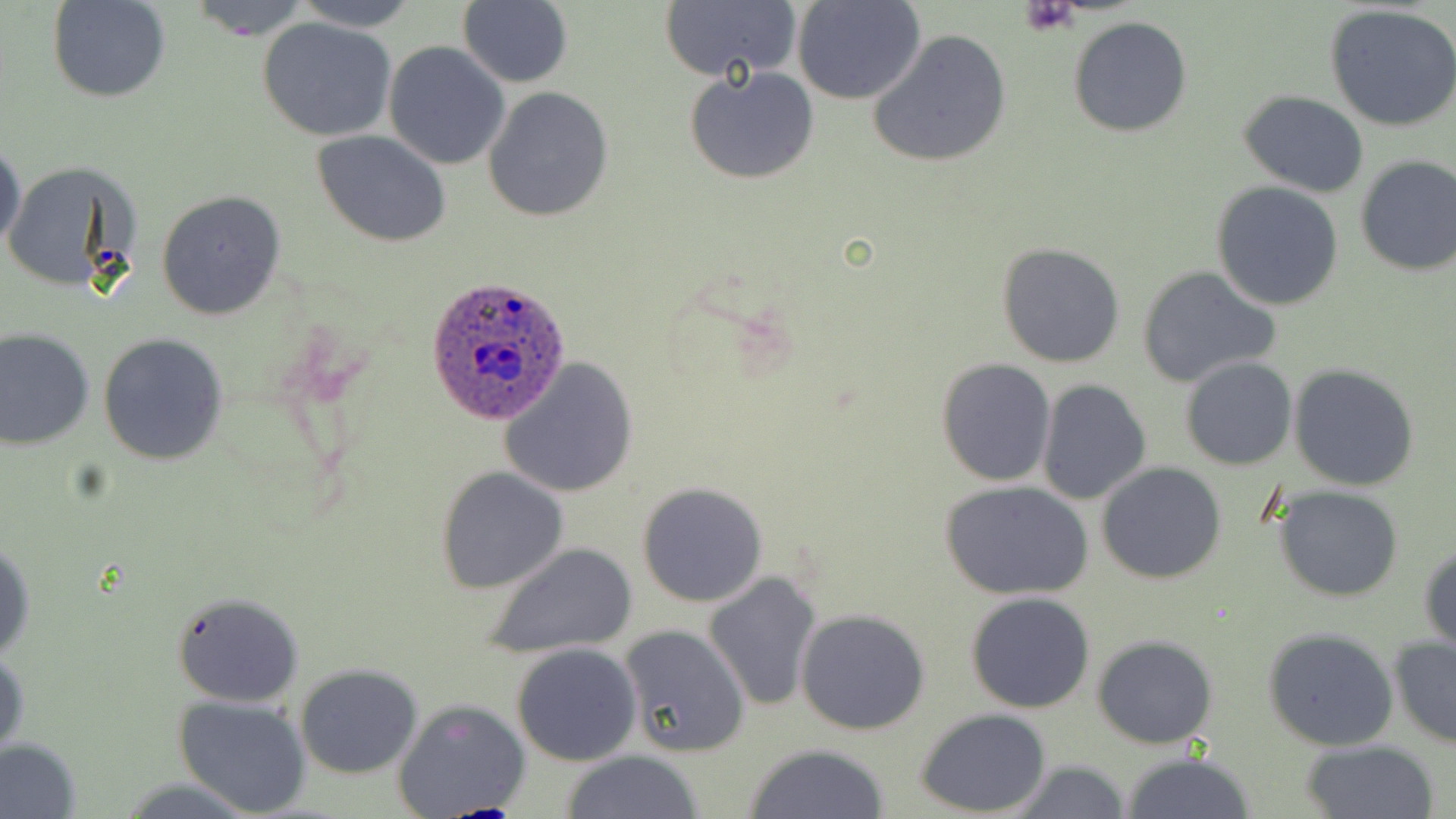
Summary:
  - Coordinate format: approximate bounding boxes as named x1/y1/x2/y2 corners in pixels
  - Uninfected red blood cell locations: (x1=48, y1=0, x2=170, y2=103), (x1=185, y1=0, x2=312, y2=37), (x1=291, y1=0, x2=423, y2=31), (x1=659, y1=0, x2=802, y2=84), (x1=794, y1=0, x2=926, y2=104), (x1=458, y1=2, x2=572, y2=87), (x1=1326, y1=6, x2=1456, y2=132), (x1=256, y1=15, x2=397, y2=141), (x1=1067, y1=16, x2=1194, y2=138), (x1=867, y1=28, x2=1013, y2=169), (x1=383, y1=41, x2=510, y2=170), (x1=685, y1=65, x2=819, y2=185), (x1=482, y1=86, x2=614, y2=223), (x1=1237, y1=90, x2=1368, y2=197), (x1=313, y1=129, x2=452, y2=247), (x1=0, y1=137, x2=26, y2=261), (x1=1353, y1=153, x2=1456, y2=275), (x1=2, y1=160, x2=140, y2=293), (x1=1211, y1=182, x2=1345, y2=312), (x1=157, y1=190, x2=287, y2=321), (x1=996, y1=242, x2=1126, y2=369), (x1=1135, y1=264, x2=1281, y2=390), (x1=0, y1=327, x2=95, y2=450), (x1=99, y1=333, x2=229, y2=465), (x1=499, y1=356, x2=639, y2=499), (x1=1181, y1=357, x2=1296, y2=470), (x1=935, y1=359, x2=1056, y2=485), (x1=1289, y1=364, x2=1420, y2=492), (x1=1036, y1=378, x2=1152, y2=505), (x1=1096, y1=462, x2=1227, y2=585), (x1=434, y1=467, x2=569, y2=594), (x1=941, y1=480, x2=1095, y2=602), (x1=637, y1=482, x2=768, y2=607), (x1=1271, y1=485, x2=1406, y2=603), (x1=484, y1=541, x2=637, y2=661), (x1=0, y1=542, x2=36, y2=664), (x1=1419, y1=542, x2=1456, y2=655), (x1=702, y1=571, x2=823, y2=713), (x1=966, y1=592, x2=1096, y2=712), (x1=171, y1=593, x2=303, y2=707), (x1=796, y1=608, x2=931, y2=735), (x1=616, y1=625, x2=749, y2=757), (x1=1263, y1=628, x2=1399, y2=751), (x1=1091, y1=633, x2=1218, y2=749), (x1=1388, y1=635, x2=1456, y2=749), (x1=512, y1=643, x2=642, y2=766), (x1=1, y1=644, x2=27, y2=765), (x1=294, y1=663, x2=423, y2=778), (x1=172, y1=696, x2=311, y2=817), (x1=392, y1=698, x2=530, y2=817), (x1=914, y1=708, x2=1053, y2=817), (x1=0, y1=737, x2=83, y2=818), (x1=1299, y1=738, x2=1442, y2=819), (x1=744, y1=744, x2=893, y2=819), (x1=561, y1=750, x2=706, y2=818), (x1=1119, y1=751, x2=1259, y2=819), (x1=1003, y1=759, x2=1133, y2=819)
  - Platelet locations: (x1=1022, y1=1, x2=1081, y2=34)
  - Plasmodium ovale-infected red blood cell locations: (x1=427, y1=275, x2=571, y2=425)
  - Slide-level diagnosis: Plasmodium ovale
  - Stain: May-Grünwald-Giemsa
  - Image size: 1456×819 pixels
  - Preparation: thin blood smear
  - Magnification: 1000x
  - Modality: light microscopy
  - Field of view: one of a larger specimen